Classify this cell by malaria status.
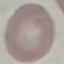
It is uninfected.

preparation = thin blood film
stain = Giemsa
capture = smartphone through the microscope eyepiece
image type = cell patch, automatically extracted from a larger field of view and resized to 64 × 64 pixels